Identify the blood parasite species.
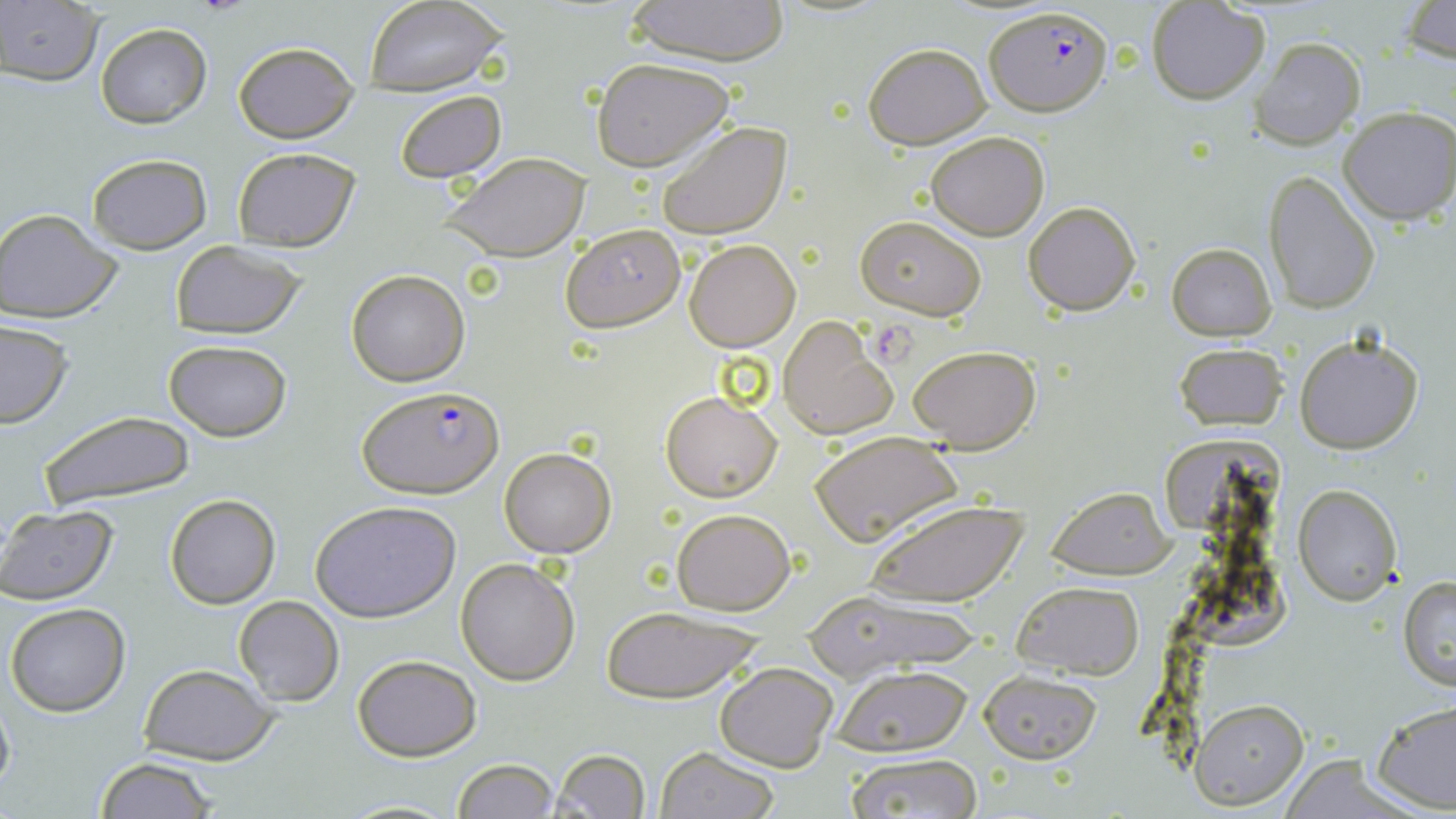
Plasmodium falciparum.

Summary:
  - Coordinate format: approximate bounding boxes as [x1, y1, x2, y2] in pixels
  - Plasmodium falciparum-infected red blood cell locations: [984, 5, 1112, 118], [359, 385, 504, 499]
  - Uninfected red blood cell locations: [1401, 0, 1456, 65], [362, 1, 509, 95], [621, 1, 794, 66], [1147, 1, 1271, 104], [0, 3, 102, 85], [96, 24, 211, 128], [1248, 37, 1366, 152], [231, 39, 360, 144], [863, 42, 991, 149], [591, 57, 737, 170], [393, 90, 505, 184], [1337, 105, 1455, 223], [656, 121, 791, 241], [926, 131, 1049, 240], [231, 146, 361, 252], [85, 152, 212, 255], [440, 152, 592, 264], [1263, 172, 1380, 314], [1024, 201, 1141, 315], [0, 208, 124, 323], [855, 216, 986, 320], [560, 222, 686, 332], [683, 239, 800, 351], [169, 240, 306, 338], [1167, 242, 1277, 340], [346, 269, 470, 386], [776, 318, 897, 440], [0, 321, 73, 429], [1294, 333, 1424, 454], [162, 339, 292, 441], [1174, 343, 1288, 431], [907, 345, 1040, 454], [661, 391, 782, 501], [38, 410, 198, 512], [809, 430, 962, 545], [498, 447, 616, 558], [1294, 483, 1401, 605], [1047, 489, 1175, 579], [165, 494, 281, 609], [864, 499, 1029, 606], [311, 500, 461, 622], [0, 505, 118, 605], [671, 506, 796, 615], [456, 557, 580, 685], [1398, 575, 1456, 691], [1010, 580, 1144, 678], [805, 591, 989, 677], [232, 596, 344, 707], [5, 602, 130, 717], [596, 603, 766, 703], [353, 654, 482, 761], [714, 661, 838, 770], [136, 663, 283, 764], [829, 666, 973, 757], [980, 670, 1102, 764], [0, 693, 15, 801], [1370, 698, 1456, 815], [1190, 699, 1309, 807], [654, 747, 779, 819], [551, 748, 651, 819], [843, 753, 983, 818], [94, 758, 218, 818], [454, 759, 558, 818], [330, 798, 464, 817]
  - Image size: 1456×819 pixels
  - Magnification: 1000x
  - Field of view: single
  - Modality: light microscopy
  - Stain: May-Grünwald-Giemsa
  - Preparation: thin blood smear